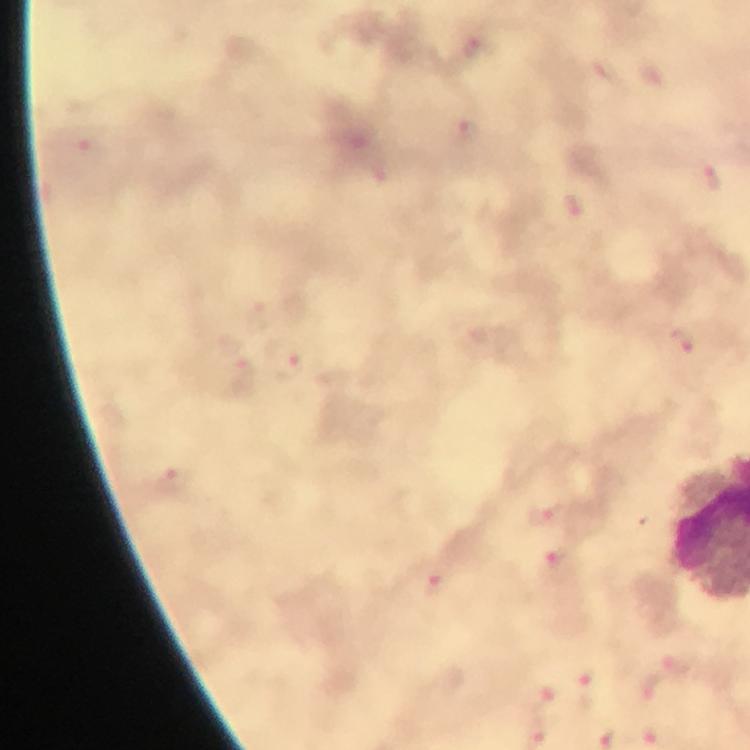
Approximate centers as [x, y] in pixels.
Summary:
  - Malaria parasite locations: [683, 342], [282, 357], [176, 480], [556, 560], [434, 584]
  - Stain: Giemsa
  - Preparation: thick blood film
  - Magnification: 100x
  - Capture: smartphone photograph through a microscope
  - Context: from a malaria diagnostic workup
  - Cropped from: a single field of view
  - Immersion oil: applied
  - Image size: 750×750 pixels